Describe the morphology of the red blood cells.
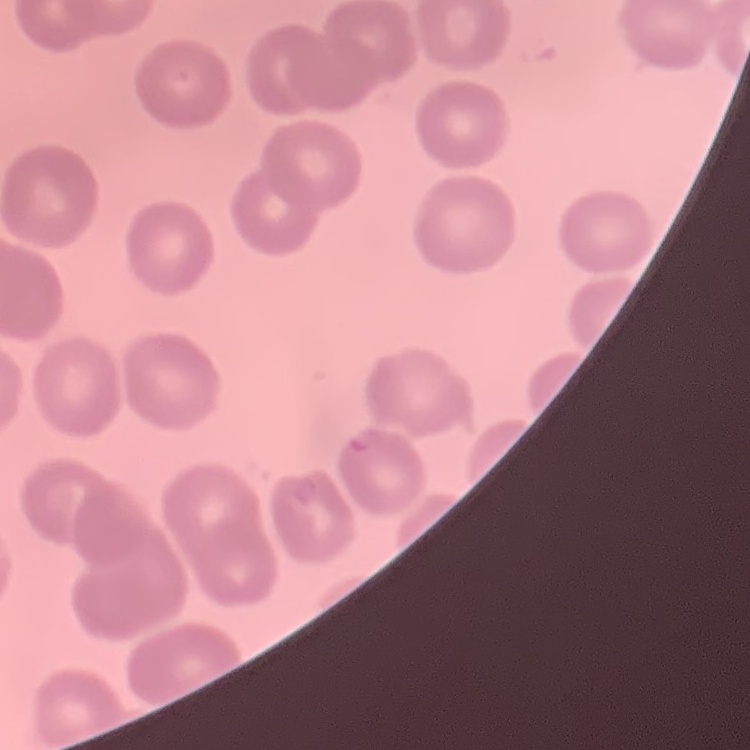
No rouleaux formation.

Summary:
  - Stain: Field's or Giemsa
  - Image type: square crop of a larger photomicrograph
  - Preparation: thin blood film